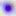 Photomicrograph. 400x magnification. Toxoplasma gondii is shown.